Assess this cell for malaria.
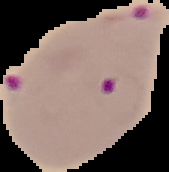
Parasitized.

Summary:
  - Preparation: thin blood smear
  - Image size: 169×172 pixels
  - Image type: segmented cell region with the area outside set to black